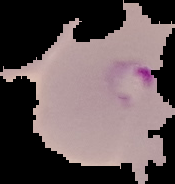

Summary:
  - Image type: cell region segmented out of the field of view; surrounding area masked to black
  - Preparation: thin blood smear
  - Image size: 175×184 pixels
  - Result: malaria parasites detected